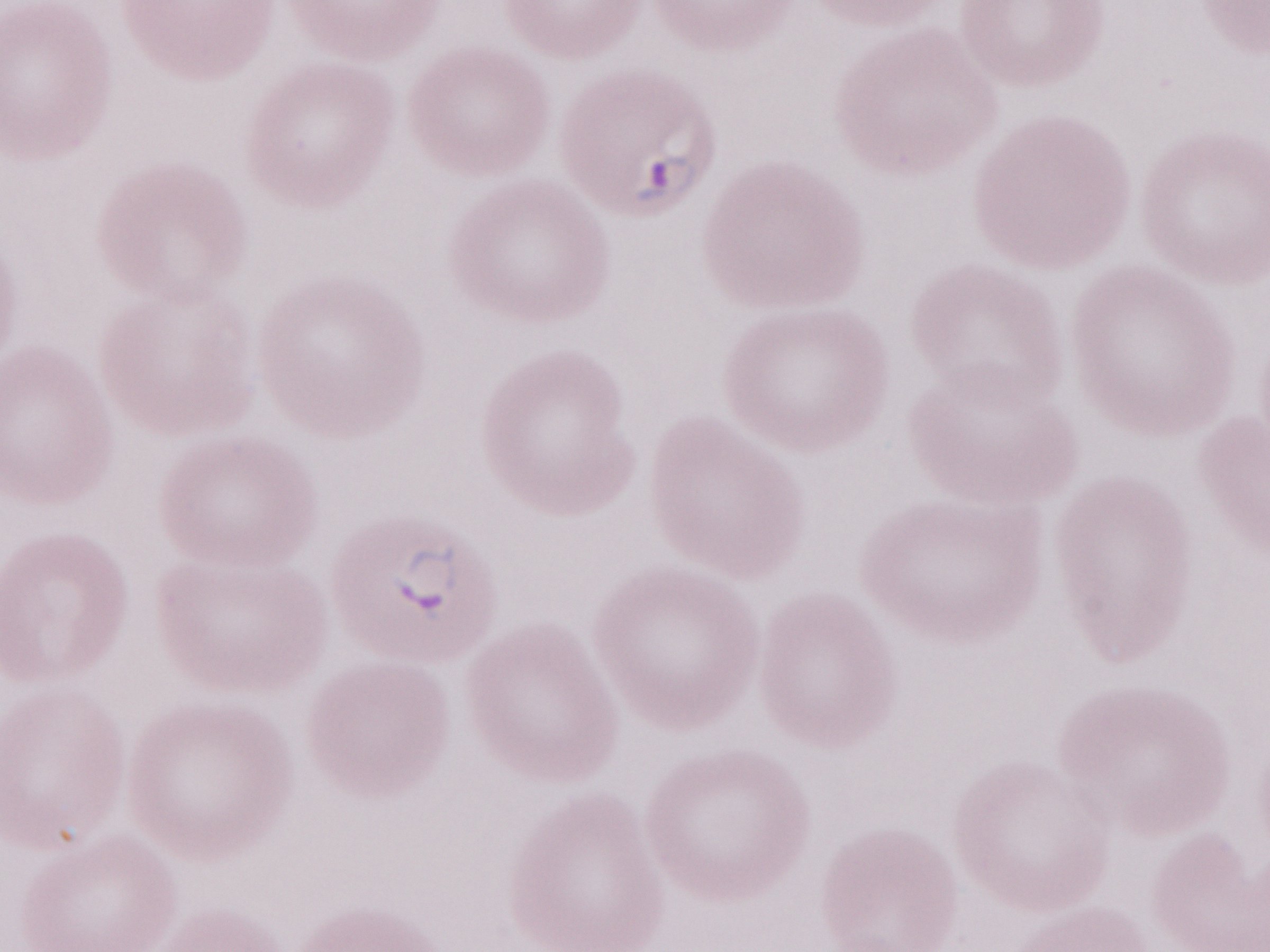 Single field of view. Magnification: 1,000x. May-Grünwald-Giemsa-stained preparation. Thin blood smear. Image is 1270×952 pixels. Patient-level malaria diagnosis: positive. Olympus BX43 microscope, Olympus DP73 camera.